Locate every Plasmodium parasite.
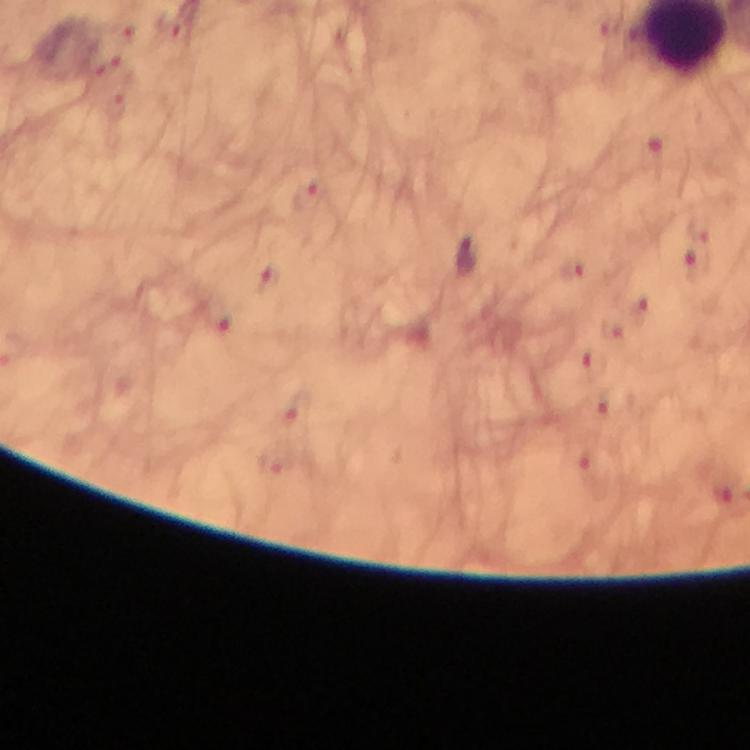
Approximate object centers, in pixels from the top-left corner.
Plasmodium parasites: (x=466, y=255), (x=700, y=268), (x=615, y=330).

From a diagnostic examination for malaria. Giemsa stain. A crop from one field of view. 100x magnification. Thick blood film. Immersion oil applied. Image is 750×750 pixels. Photographed through the microscope with a smartphone camera.